Locate the cells, classifying each as a parasitized RBC, an uninfected RBC, or a WBC.
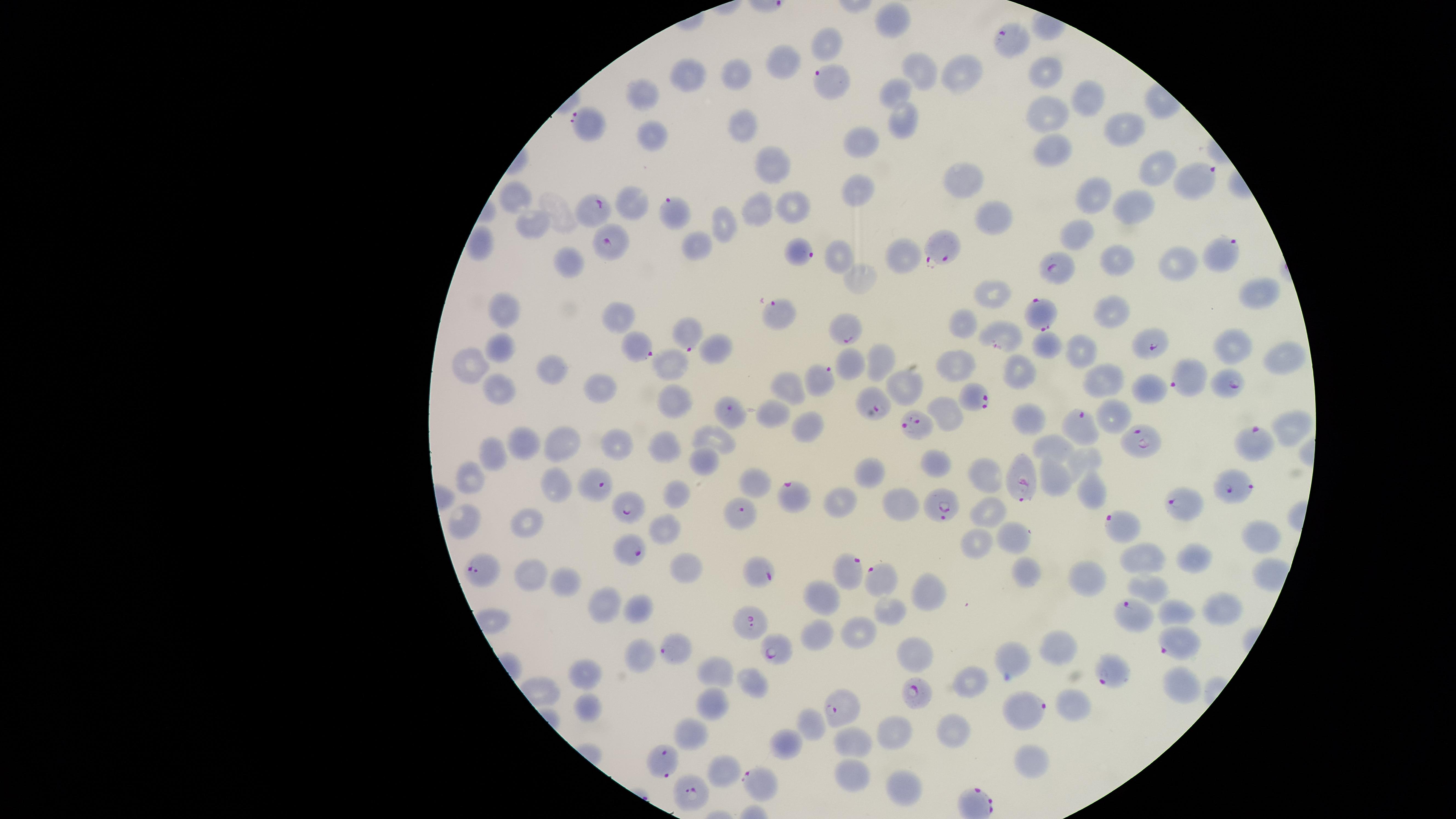
Approximate marker points as {x, y} in pixels.
Parasitized RBCs: {1008, 41}, {831, 87}, {589, 123}, {1197, 179}, {595, 209}, {675, 214}, {614, 242}, {942, 248}, {799, 251}, {1220, 252}, {1056, 268}, {1042, 310}, {779, 311}, {841, 327}, {691, 333}, {1147, 344}, {639, 345}, {1185, 377}, {817, 380}, {1231, 387}, {974, 398}, {877, 405}, {731, 412}, {918, 425}, {1081, 426}, {1142, 440}, {1255, 442}, {1026, 481}, {1228, 484}, {596, 485}, {791, 494}, {943, 504}, {1182, 505}, {629, 512}, {741, 514}, {1119, 523}, {633, 550}, {477, 569}, {760, 573}, {847, 573}, {877, 576}, {1128, 612}, {747, 621}, {1174, 640}, {674, 651}, {780, 651}, {1109, 674}, {915, 693}, {1025, 712}, {842, 713}, {661, 763}, {761, 780}, {688, 795}.
Uninfected RBCs: {895, 16}, {825, 43}, {780, 63}, {918, 69}, {1045, 69}, {686, 73}, {735, 73}, {962, 73}, {899, 92}, {1084, 94}, {641, 96}, {1046, 111}, {742, 122}, {901, 124}, {1124, 124}, {648, 135}, {859, 140}, {1056, 149}, {769, 162}, {1151, 167}, {959, 179}, {859, 189}, {1094, 192}, {515, 195}, {635, 201}, {790, 202}, {1136, 205}, {754, 206}, {986, 213}, {528, 225}, {724, 227}, {1084, 234}, {482, 240}, {697, 244}, {900, 254}, {840, 255}, {1116, 259}, {568, 260}, {1175, 265}, {859, 274}, {1258, 291}, {990, 294}, {1112, 308}, {506, 312}, {619, 318}, {963, 319}, {999, 328}, {1046, 341}, {716, 345}, {498, 346}, {1082, 348}, {1231, 349}, {1280, 352}, {877, 358}, {469, 361}, {552, 366}, {669, 366}, {850, 366}, {950, 366}, {1021, 373}, {790, 381}, {1106, 383}, {598, 386}, {498, 388}, {906, 389}, {1151, 389}, {673, 402}, {943, 408}, {773, 414}, {1032, 418}, {1291, 423}, {808, 428}, {560, 441}, {616, 441}, {714, 442}, {519, 443}, {664, 443}, {1050, 446}, {492, 452}, {692, 459}, {1082, 460}, {934, 462}, {469, 472}, {874, 473}, {1056, 475}, {985, 476}, {747, 478}, {556, 485}, {1088, 489}, {672, 491}, {844, 498}, {901, 499}, {985, 509}, {525, 518}, {459, 523}, {659, 529}, {1014, 532}, {1260, 532}, {971, 540}, {1138, 551}, {1196, 557}, {683, 566}, {530, 573}, {1024, 574}, {1088, 578}, {923, 582}, {566, 583}, {1146, 586}, {820, 592}, {602, 601}, {636, 603}, {1225, 606}, {883, 608}, {1177, 609}, {853, 632}, {815, 635}, {1060, 647}, {636, 651}, {913, 654}, {1017, 655}, {580, 669}, {715, 670}, {968, 679}, {745, 681}, {1180, 690}, {586, 703}, {1071, 705}, {707, 706}, {809, 722}, {690, 729}, {893, 729}, {951, 729}, {784, 742}, {854, 743}, {1031, 762}, {721, 766}, {846, 775}, {899, 786}.
No WBCs identified.

Summary:
  - Field of view: single
  - Preparation: thin blood smear
  - Species: Plasmodium falciparum
  - Visible region: circular
  - Image size: 1456×819 pixels
  - Stain: Giemsa
  - Capture: smartphone photograph through the microscope eyepiece